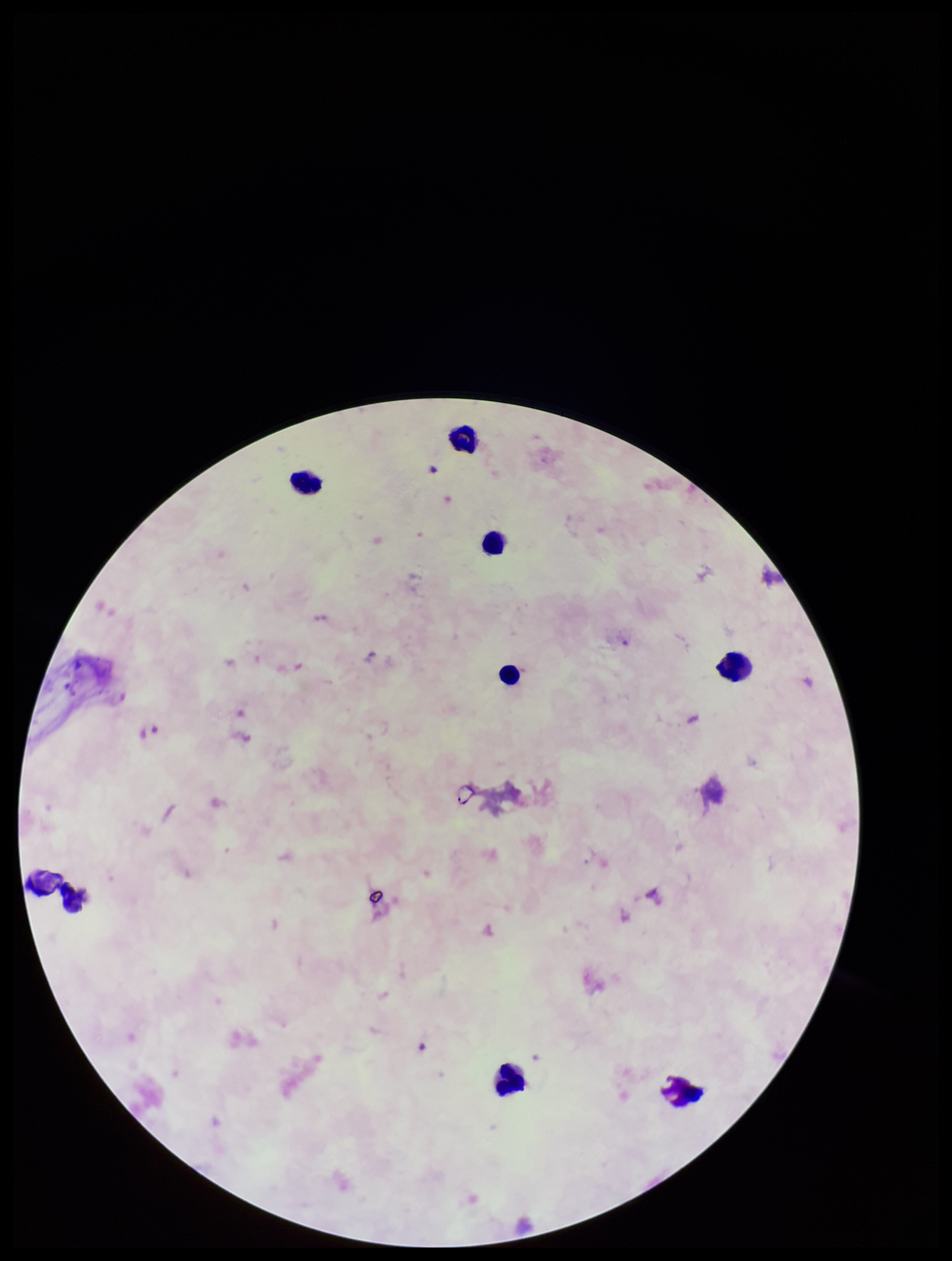
Summary:
  - Image size: 952×1261 pixels
  - Parasite count: 0
  - Patient malaria status: negative
  - Preparation: thick
  - Plasmodium parasites: none detected
  - Capture: smartphone photograph through the microscope eyepiece
  - Stain: Giemsa
  - Leukocyte count: 8
  - Field of view: single